Report the malaria status of this cell.
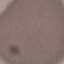

It is uninfected.

{
  "preparation": "thin blood smear",
  "image_type": "cell patch, automatically extracted from a larger field of view and resized to 64 × 64 pixels",
  "stain": "Giemsa",
  "capture": "smartphone camera at the microscope eyepiece"
}